Evaluate for Plasmodium parasites.
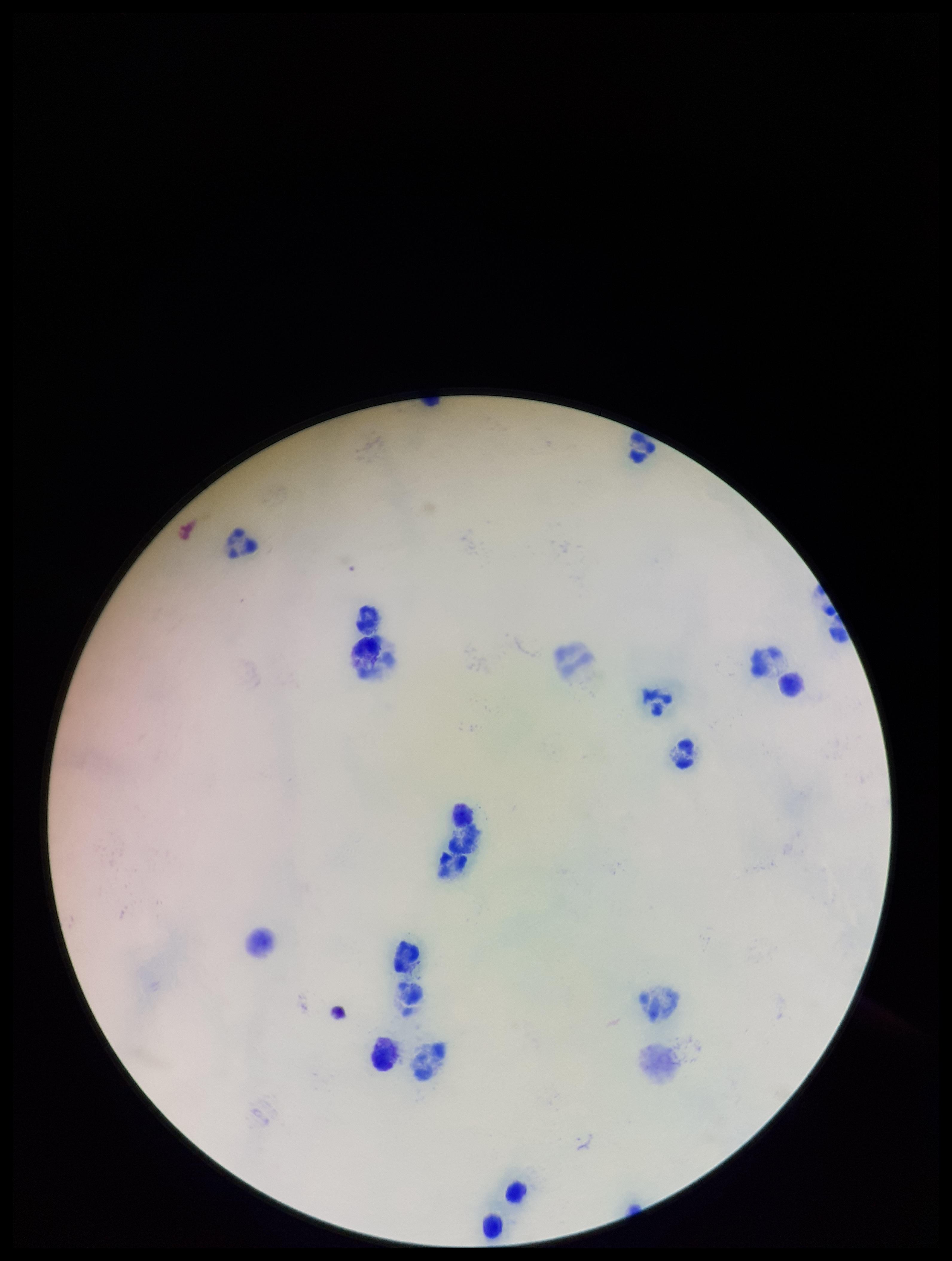

None seen.

Summary:
  - Image size: 952×1261 pixels
  - Capture: smartphone photograph through the microscope eyepiece
  - Patient malaria status: negative
  - Leukocyte count: 15
  - Field of view: single
  - Parasite count: 0
  - Preparation: thick
  - Stain: Giemsa